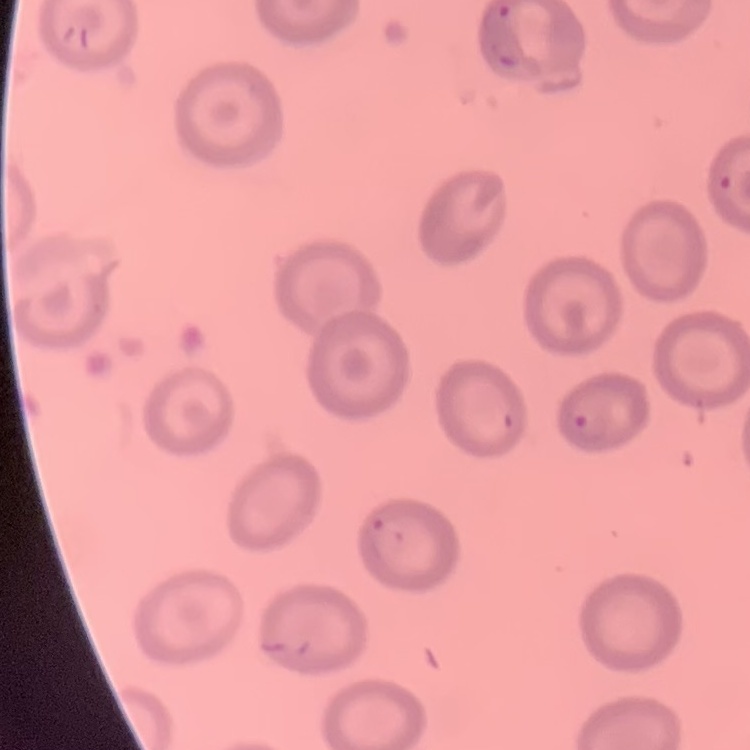
{
  "erythrocyte_morphology": "no rouleaux formation",
  "preparation": "thin blood film",
  "stain": "Field's or Giemsa",
  "image_type": "square crop of a larger photomicrograph"
}